Mark where platelets are.
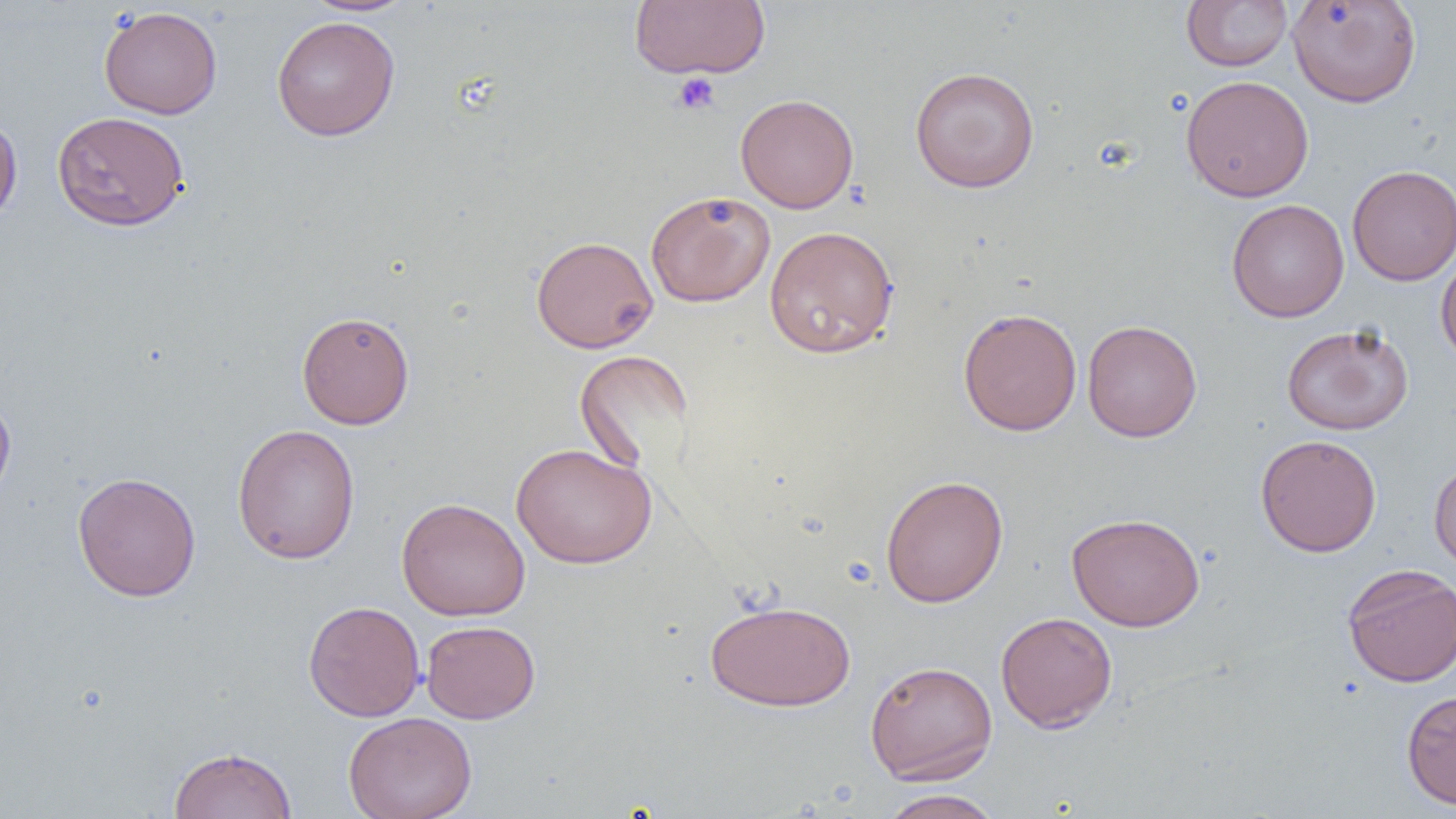

Approximate bounding boxes as [x1, y1, x2, y2] in pixels.
Platelets: [672, 72, 721, 115].

Summary:
  - Uninfected red blood cell locations: [303, 0, 418, 16], [1287, 0, 1422, 108], [629, 1, 771, 79], [1181, 1, 1293, 71], [98, 5, 223, 119], [272, 15, 400, 141], [909, 66, 1040, 193], [1180, 75, 1314, 202], [735, 93, 859, 213], [52, 111, 189, 231], [0, 113, 23, 225], [1346, 165, 1456, 286], [645, 190, 775, 307], [1226, 199, 1350, 322], [764, 225, 899, 358], [531, 235, 659, 353], [1435, 250, 1456, 367], [958, 307, 1082, 436], [296, 311, 415, 429], [1082, 319, 1202, 443], [1281, 323, 1413, 435], [574, 350, 694, 476], [0, 389, 16, 506], [231, 423, 361, 565], [1256, 434, 1382, 557], [511, 442, 657, 569], [1429, 458, 1456, 574], [72, 471, 201, 602], [880, 474, 1008, 608], [396, 497, 530, 621], [1066, 512, 1205, 631], [1342, 563, 1456, 687], [704, 598, 857, 711], [303, 600, 425, 722], [995, 611, 1117, 733], [421, 620, 540, 723], [865, 659, 998, 784], [1401, 689, 1456, 809], [343, 711, 477, 819], [168, 746, 298, 819], [877, 790, 1005, 819]
  - Slide-level diagnosis: no evidence of blood parasites
  - Modality: light microscopy
  - Image size: 1456×819 pixels
  - Preparation: thin blood smear
  - Magnification: 1000x
  - Field of view: single